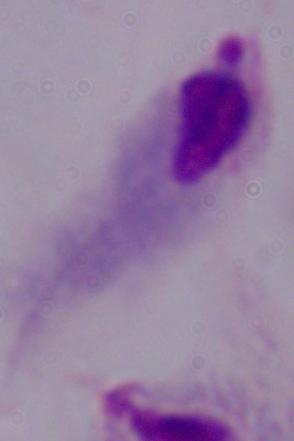

magnification = 1000x
modality = micrograph
identification = trichomonad